Classify this cell by malaria status.
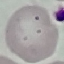
It is uninfected.

capture: smartphone through the microscope eyepiece
preparation: thin blood film
stain: Giemsa
image_type: cell patch, automatically extracted from a larger field of view and resized to 64 × 64 pixels